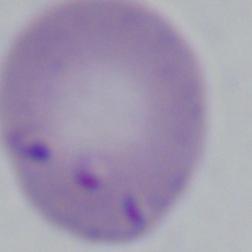
Summary:
  - Modality: micrograph
  - Identification: Babesia
  - Magnification: 1000x